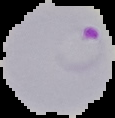
image_size: 115×118 pixels
result: malaria parasites detected
image_type: cell region segmented out of the field of view; surrounding area masked to black
preparation: thin blood film